Classify this cell by malaria status.
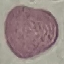
It is uninfected.

capture = smartphone through the microscope eyepiece
stain = Giemsa
image type = cell patch, automatically extracted from a larger field of view and resized to 64 × 64 pixels
preparation = thin blood smear